Locate and identify every blood parasite.
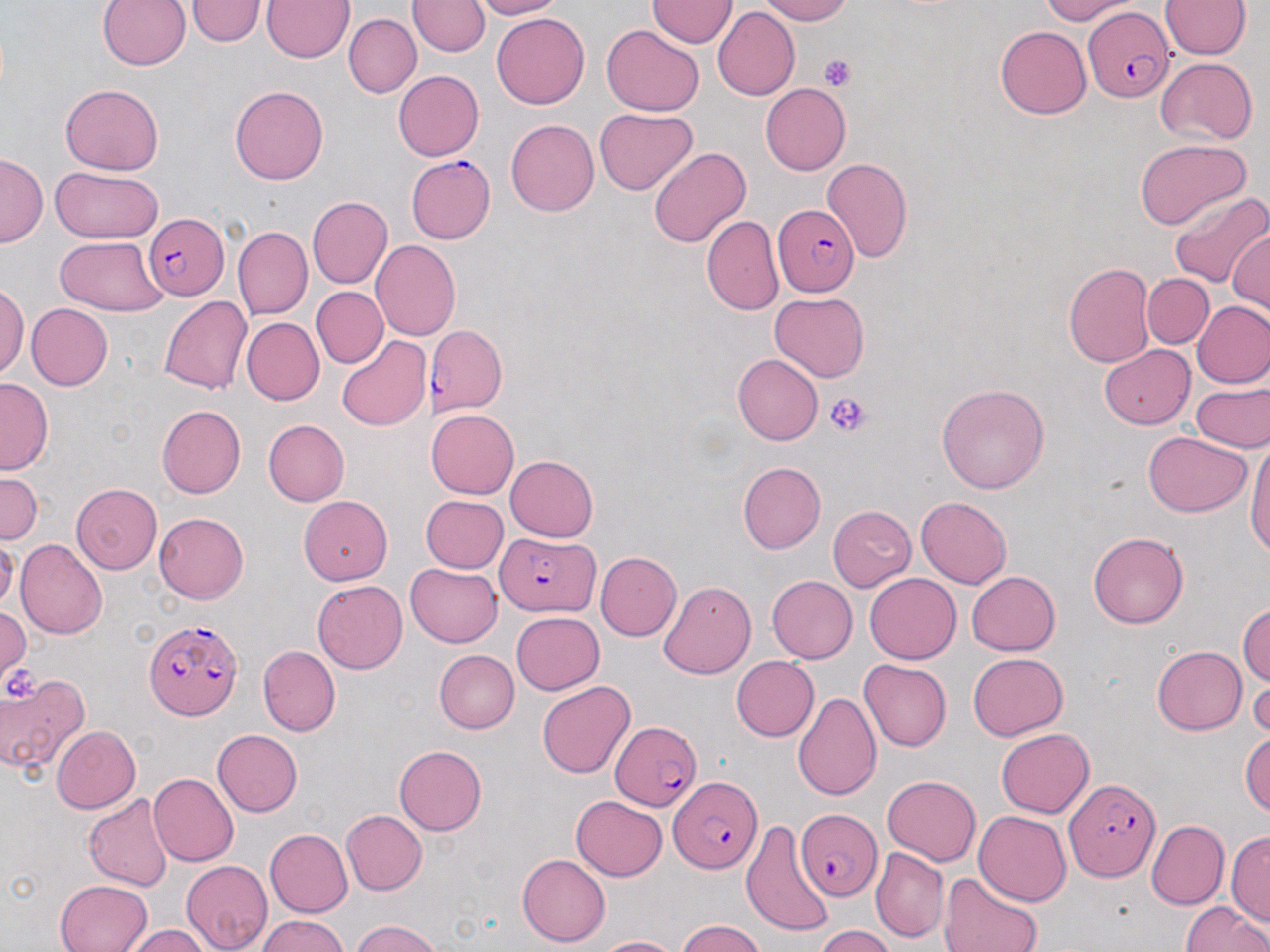
Approximate bounding boxes as named x1/y1/x2/y2 corners in pixels.
Plasmodium falciparum-infected red blood cells: (x1=1081, y1=8, x2=1175, y2=102), (x1=404, y1=155, x2=496, y2=245), (x1=774, y1=204, x2=860, y2=297), (x1=142, y1=212, x2=227, y2=299), (x1=425, y1=325, x2=507, y2=416), (x1=495, y1=533, x2=599, y2=616), (x1=143, y1=614, x2=244, y2=723), (x1=610, y1=720, x2=702, y2=811), (x1=671, y1=776, x2=763, y2=874), (x1=1065, y1=776, x2=1161, y2=879), (x1=797, y1=810, x2=882, y2=901).
No Plasmodium ovale, Plasmodium malariae, Plasmodium vivax, Babesia divergens, or Trypanosoma brucei observed.

Summary:
  - Uninfected red blood cell locations: (x1=98, y1=0, x2=191, y2=72), (x1=188, y1=0, x2=262, y2=47), (x1=261, y1=0, x2=353, y2=63), (x1=470, y1=0, x2=566, y2=20), (x1=755, y1=0, x2=857, y2=24), (x1=1034, y1=0, x2=1138, y2=23), (x1=410, y1=1, x2=487, y2=57), (x1=648, y1=1, x2=735, y2=48), (x1=1161, y1=1, x2=1248, y2=59), (x1=711, y1=7, x2=798, y2=101), (x1=490, y1=12, x2=590, y2=109), (x1=346, y1=13, x2=420, y2=97), (x1=601, y1=23, x2=703, y2=115), (x1=995, y1=26, x2=1091, y2=119), (x1=1154, y1=57, x2=1259, y2=146), (x1=392, y1=71, x2=483, y2=161), (x1=60, y1=84, x2=165, y2=174), (x1=761, y1=85, x2=851, y2=174), (x1=230, y1=86, x2=329, y2=184), (x1=595, y1=107, x2=696, y2=195), (x1=505, y1=117, x2=599, y2=217), (x1=1134, y1=139, x2=1252, y2=227), (x1=650, y1=146, x2=749, y2=246), (x1=1, y1=154, x2=44, y2=246), (x1=819, y1=158, x2=912, y2=264), (x1=49, y1=167, x2=164, y2=241), (x1=1166, y1=187, x2=1269, y2=290), (x1=309, y1=196, x2=391, y2=288), (x1=702, y1=215, x2=783, y2=316), (x1=1229, y1=224, x2=1269, y2=317), (x1=234, y1=226, x2=311, y2=319), (x1=55, y1=237, x2=164, y2=315), (x1=370, y1=240, x2=462, y2=339), (x1=1062, y1=262, x2=1152, y2=370), (x1=1144, y1=273, x2=1213, y2=348), (x1=0, y1=282, x2=27, y2=378), (x1=311, y1=287, x2=386, y2=367), (x1=768, y1=292, x2=869, y2=382), (x1=161, y1=295, x2=252, y2=396), (x1=1192, y1=300, x2=1270, y2=389), (x1=25, y1=303, x2=112, y2=390), (x1=240, y1=317, x2=323, y2=405), (x1=335, y1=335, x2=431, y2=431), (x1=1099, y1=342, x2=1195, y2=428), (x1=733, y1=355, x2=822, y2=444), (x1=1, y1=379, x2=50, y2=473), (x1=937, y1=383, x2=1048, y2=497), (x1=1190, y1=385, x2=1270, y2=454), (x1=156, y1=404, x2=245, y2=499), (x1=424, y1=409, x2=519, y2=498), (x1=263, y1=419, x2=349, y2=505), (x1=1142, y1=432, x2=1253, y2=518), (x1=1246, y1=435, x2=1270, y2=568), (x1=505, y1=454, x2=599, y2=540), (x1=738, y1=461, x2=826, y2=553), (x1=0, y1=471, x2=42, y2=542), (x1=71, y1=485, x2=163, y2=575), (x1=297, y1=495, x2=389, y2=583), (x1=420, y1=495, x2=508, y2=574), (x1=916, y1=497, x2=1011, y2=588), (x1=827, y1=506, x2=916, y2=589), (x1=153, y1=512, x2=249, y2=603), (x1=1088, y1=531, x2=1188, y2=628), (x1=0, y1=536, x2=18, y2=610), (x1=16, y1=539, x2=108, y2=640), (x1=597, y1=552, x2=681, y2=641), (x1=406, y1=562, x2=502, y2=646), (x1=865, y1=571, x2=960, y2=660), (x1=965, y1=571, x2=1061, y2=655), (x1=767, y1=575, x2=857, y2=662), (x1=658, y1=579, x2=755, y2=679), (x1=312, y1=580, x2=406, y2=674), (x1=1237, y1=601, x2=1270, y2=689), (x1=0, y1=605, x2=29, y2=679), (x1=512, y1=610, x2=605, y2=694), (x1=1151, y1=643, x2=1247, y2=734), (x1=257, y1=645, x2=338, y2=738), (x1=435, y1=650, x2=520, y2=733), (x1=967, y1=652, x2=1068, y2=741), (x1=731, y1=657, x2=820, y2=742), (x1=860, y1=657, x2=953, y2=752), (x1=0, y1=668, x2=93, y2=776), (x1=537, y1=679, x2=635, y2=780), (x1=1249, y1=679, x2=1270, y2=740), (x1=792, y1=690, x2=881, y2=802), (x1=54, y1=726, x2=143, y2=815), (x1=213, y1=729, x2=303, y2=817), (x1=996, y1=729, x2=1094, y2=815), (x1=1240, y1=729, x2=1269, y2=817), (x1=392, y1=745, x2=485, y2=836), (x1=149, y1=773, x2=238, y2=866), (x1=882, y1=776, x2=978, y2=865), (x1=84, y1=794, x2=172, y2=888), (x1=571, y1=796, x2=667, y2=880), (x1=974, y1=808, x2=1071, y2=904), (x1=341, y1=809, x2=427, y2=895), (x1=742, y1=814, x2=836, y2=940), (x1=1146, y1=818, x2=1228, y2=910), (x1=265, y1=828, x2=352, y2=918), (x1=1228, y1=833, x2=1269, y2=927), (x1=871, y1=848, x2=947, y2=941), (x1=517, y1=853, x2=610, y2=945), (x1=180, y1=859, x2=273, y2=950), (x1=939, y1=871, x2=1045, y2=952), (x1=54, y1=879, x2=151, y2=952), (x1=1180, y1=899, x2=1269, y2=952), (x1=254, y1=915, x2=349, y2=952), (x1=349, y1=919, x2=444, y2=952), (x1=674, y1=922, x2=771, y2=952), (x1=810, y1=924, x2=895, y2=951), (x1=128, y1=926, x2=213, y2=952), (x1=591, y1=934, x2=681, y2=952)
  - Platelet locations: (x1=820, y1=55, x2=857, y2=91), (x1=827, y1=394, x2=869, y2=437), (x1=4, y1=663, x2=45, y2=703)
  - Slide-level diagnosis: Plasmodium falciparum
  - Stain: May-Grünwald-Giemsa
  - Image size: 1270×952 pixels
  - Magnification: 1000x
  - Modality: light microscopy
  - Preparation: thin blood smear
  - Field of view: one of a larger specimen